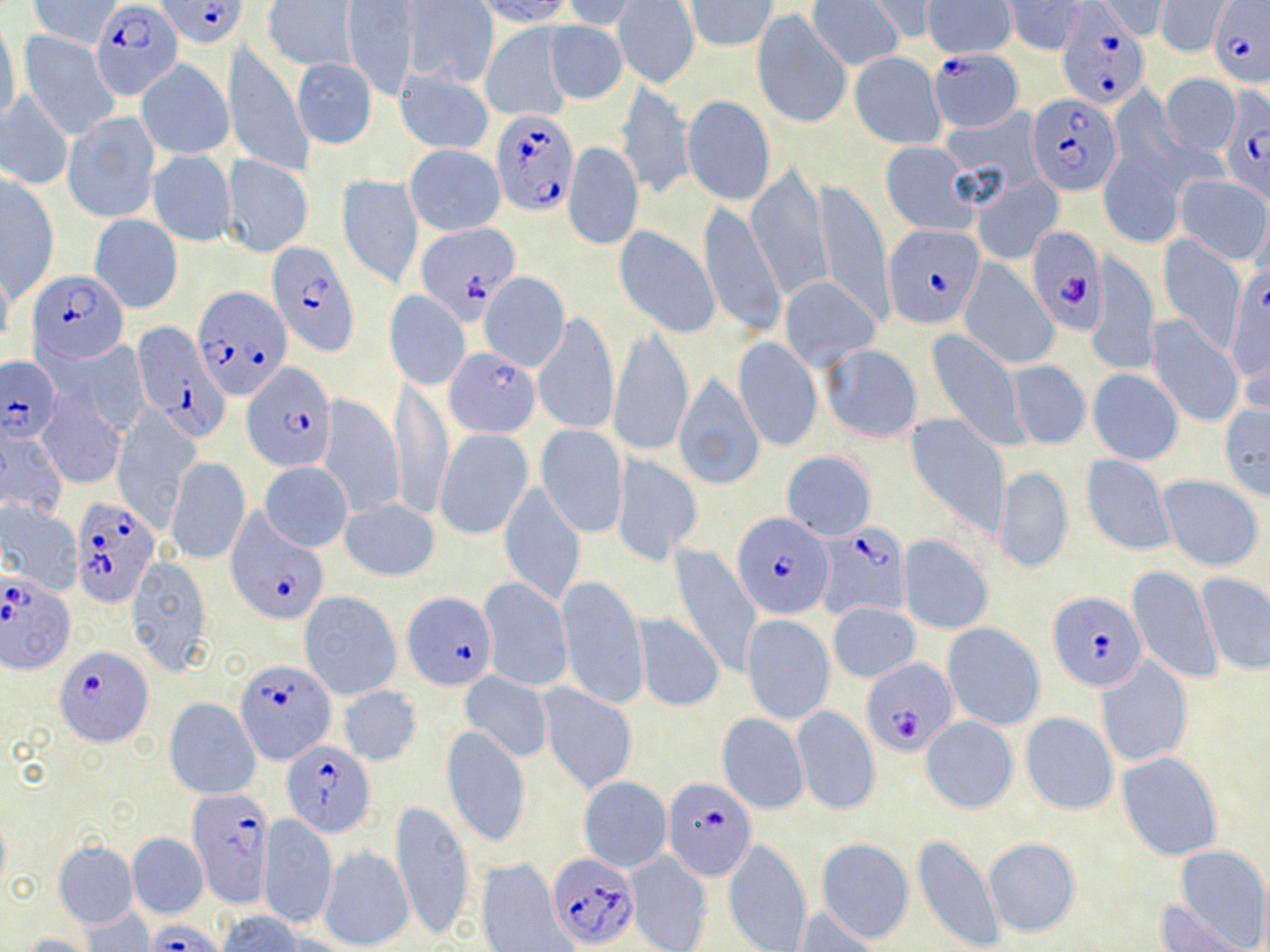
Approximate bounding boxes as (x1, y1, x2, y2) in pixels. Uninfected red blood cell locations: (32, 0, 119, 48), (262, 0, 355, 71), (477, 0, 577, 27), (559, 0, 638, 29), (867, 0, 938, 41), (684, 1, 777, 51), (807, 1, 902, 71), (924, 1, 1014, 58), (1005, 1, 1084, 55), (1094, 1, 1169, 40), (344, 2, 417, 101), (613, 2, 699, 88), (1156, 2, 1228, 57), (405, 3, 497, 87), (753, 11, 849, 128), (0, 19, 22, 129), (543, 21, 627, 103), (480, 23, 572, 121), (18, 31, 119, 141), (225, 41, 312, 177), (850, 51, 946, 149), (136, 57, 234, 160), (292, 58, 377, 147), (396, 68, 494, 155), (1159, 73, 1241, 156), (615, 80, 693, 201), (1, 89, 73, 190), (680, 95, 777, 206), (941, 106, 1044, 205), (63, 112, 160, 224), (564, 141, 642, 250), (881, 142, 974, 233), (405, 144, 505, 235), (148, 150, 236, 247), (1098, 150, 1183, 249), (222, 155, 314, 258), (745, 165, 832, 299), (2, 173, 60, 299), (974, 175, 1063, 264), (1175, 175, 1270, 263), (337, 176, 424, 289), (815, 179, 892, 327), (698, 201, 784, 337), (90, 214, 183, 314), (614, 225, 720, 340), (1157, 235, 1246, 351), (1090, 253, 1157, 376), (958, 258, 1059, 369), (0, 260, 13, 354), (1225, 264, 1269, 390), (478, 271, 570, 371), (778, 275, 881, 371), (386, 290, 470, 389), (534, 309, 620, 438), (1146, 316, 1244, 428), (608, 327, 692, 457), (926, 328, 1027, 447), (68, 338, 150, 434), (734, 339, 821, 452), (820, 344, 922, 442), (443, 347, 539, 438), (1003, 358, 1091, 451), (1087, 369, 1183, 464), (674, 374, 765, 490), (392, 382, 452, 520), (316, 393, 405, 519), (37, 394, 126, 490), (1218, 403, 1270, 501), (111, 409, 201, 528), (908, 416, 1008, 535), (536, 424, 627, 537), (0, 426, 68, 517), (434, 428, 533, 539), (781, 451, 876, 541), (611, 453, 702, 567), (1081, 454, 1175, 555), (168, 457, 250, 564), (259, 462, 352, 552), (994, 466, 1072, 576), (1157, 476, 1263, 572), (500, 482, 585, 604), (340, 497, 440, 581), (0, 500, 83, 594), (897, 536, 991, 634), (669, 544, 762, 679), (127, 557, 211, 676), (1127, 563, 1221, 685), (1195, 572, 1270, 675), (479, 577, 572, 691), (557, 577, 648, 708), (299, 591, 401, 699), (827, 601, 920, 683), (633, 613, 724, 711), (742, 614, 834, 722), (943, 623, 1045, 730), (1096, 657, 1192, 768), (459, 671, 553, 762), (539, 682, 637, 795), (336, 684, 423, 767), (164, 698, 261, 799), (792, 705, 879, 816), (1020, 712, 1118, 814), (717, 713, 809, 814), (920, 715, 1018, 812), (442, 728, 531, 845), (1116, 752, 1222, 861), (579, 777, 672, 872), (390, 801, 474, 942), (257, 814, 337, 929), (0, 819, 10, 892), (129, 833, 208, 919), (911, 834, 1005, 952), (723, 837, 811, 952), (815, 837, 915, 944), (983, 837, 1082, 937), (54, 842, 139, 929), (319, 844, 413, 950), (1172, 845, 1269, 951), (624, 850, 712, 952), (477, 858, 576, 952), (1157, 901, 1249, 951), (82, 907, 154, 950), (791, 907, 884, 951), (215, 911, 306, 952), (21, 934, 94, 952). Plasmodium falciparum-infected red blood cell locations: (158, 0, 247, 48), (1207, 0, 1270, 88), (92, 2, 183, 99), (1055, 4, 1147, 108), (929, 49, 1023, 133), (1026, 95, 1121, 196), (1222, 101, 1270, 207), (492, 110, 576, 217), (415, 223, 519, 324), (884, 224, 984, 329), (1027, 226, 1107, 335), (269, 244, 359, 356), (29, 270, 129, 363), (193, 285, 293, 400), (131, 325, 227, 438), (1, 355, 63, 443), (245, 363, 335, 471), (71, 496, 161, 604), (225, 507, 327, 624), (734, 512, 831, 617), (816, 523, 910, 620), (1, 568, 76, 674), (402, 592, 498, 690), (1049, 593, 1148, 693), (57, 645, 153, 745), (861, 658, 958, 756), (236, 659, 336, 764), (282, 742, 374, 835), (662, 777, 756, 879), (187, 790, 272, 906), (549, 852, 637, 948), (147, 922, 227, 952). Slide-level diagnosis: Plasmodium falciparum. Captured at 1000x magnification. Optical microscopy. Image is 1270×952 pixels. Thin blood film. May-Grünwald-Giemsa stain. Single field of view.